Classify this cell by malaria status.
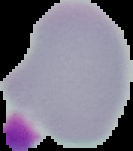

It is uninfected.

Image is 133×151 pixels. From a thin blood smear. Cell region segmented out of the field of view; the surrounding area is masked to black.